Identify the blood parasite species.
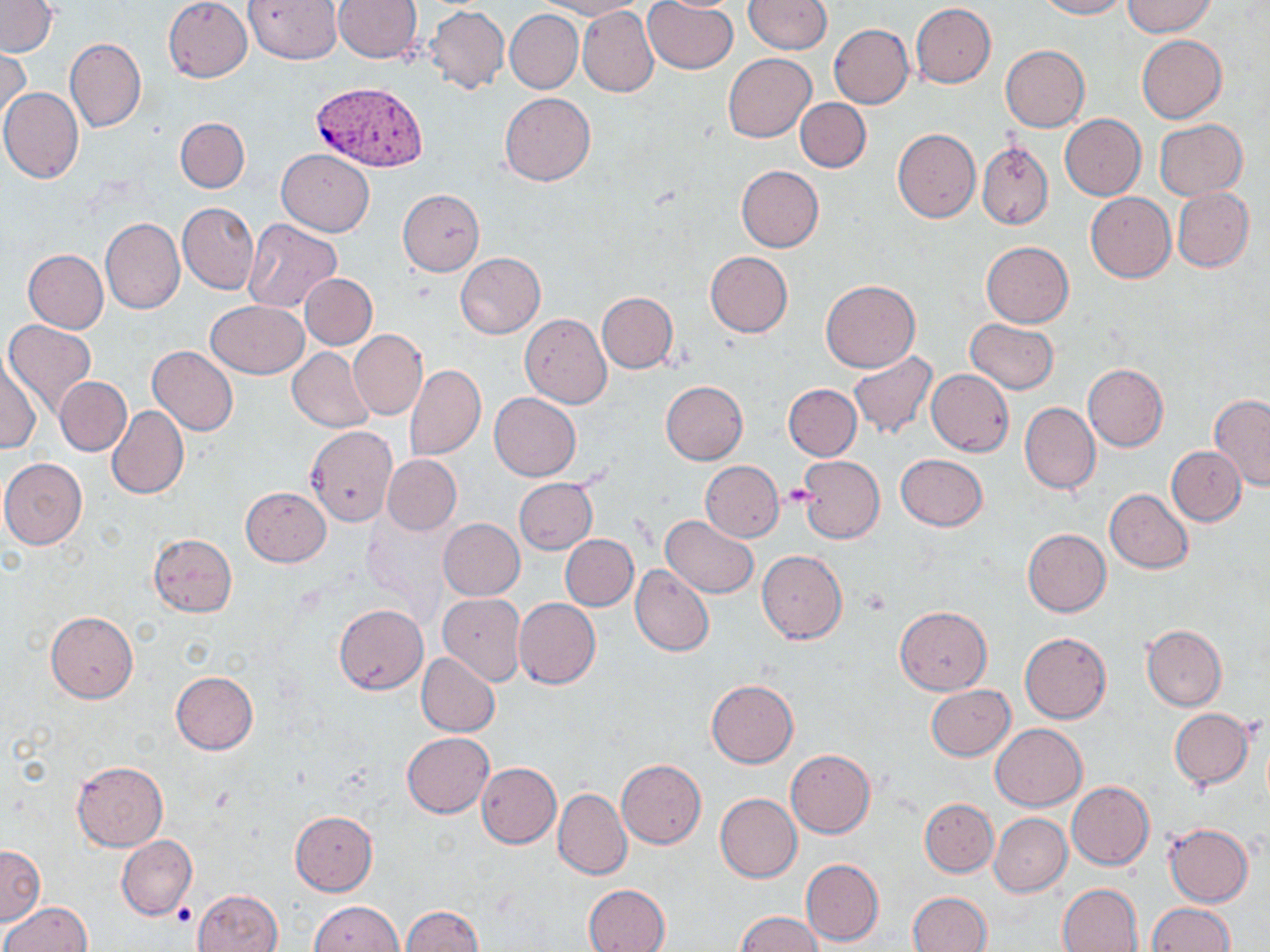

Plasmodium vivax.

uninfected red blood cell locations = approximate bounding boxes as (x1, y1, x2, y2) in pixels: (164, 0, 253, 82), (245, 0, 341, 64), (333, 0, 422, 63), (540, 0, 647, 19), (745, 0, 832, 53), (1036, 0, 1128, 19), (1123, 0, 1216, 36), (0, 1, 57, 57), (644, 1, 738, 73), (911, 3, 996, 88), (578, 5, 658, 97), (424, 6, 509, 93), (506, 10, 583, 93), (829, 24, 913, 108), (1136, 34, 1226, 122), (66, 36, 146, 132), (999, 45, 1089, 133), (1, 49, 31, 130), (723, 53, 816, 143), (0, 87, 83, 183), (499, 92, 596, 186), (796, 98, 871, 172), (1059, 114, 1145, 200), (175, 117, 250, 192), (1154, 119, 1248, 199), (893, 128, 981, 223), (977, 141, 1053, 230), (276, 149, 374, 236), (736, 165, 824, 252), (1171, 187, 1254, 271), (398, 189, 484, 276), (1086, 193, 1175, 282), (178, 202, 258, 294), (100, 217, 185, 315), (242, 219, 342, 312), (981, 242, 1074, 327), (24, 249, 108, 333), (705, 251, 793, 337), (455, 252, 545, 338), (299, 273, 377, 350), (821, 279, 919, 372), (597, 292, 677, 372), (206, 301, 308, 377), (520, 313, 612, 408), (965, 318, 1059, 393), (4, 319, 97, 416), (349, 330, 427, 420), (148, 346, 238, 435), (288, 347, 375, 433), (848, 351, 938, 440), (1, 353, 40, 455), (1082, 364, 1168, 451), (405, 365, 485, 460), (926, 370, 1014, 455), (54, 377, 131, 456), (660, 381, 747, 465), (783, 384, 862, 461), (490, 392, 581, 480), (1209, 395, 1270, 492), (1019, 402, 1100, 494), (107, 405, 188, 500), (306, 425, 399, 527), (1166, 446, 1246, 525), (896, 452, 987, 532), (382, 454, 461, 535), (798, 455, 886, 542), (0, 458, 87, 549), (700, 461, 783, 542), (514, 478, 597, 555), (241, 486, 331, 566), (1104, 489, 1193, 573), (660, 516, 758, 598), (439, 519, 524, 600), (1023, 528, 1111, 616), (149, 533, 237, 616), (560, 534, 639, 611), (757, 550, 847, 644), (630, 564, 714, 656), (437, 593, 526, 686), (513, 598, 601, 689), (334, 604, 427, 694), (894, 606, 991, 695), (45, 612, 138, 703), (1141, 624, 1226, 710), (1019, 632, 1112, 724), (417, 653, 500, 737), (170, 671, 258, 755), (706, 679, 798, 768), (926, 685, 1016, 761), (1168, 708, 1254, 789), (991, 723, 1087, 810), (403, 731, 494, 817), (786, 749, 875, 838), (617, 759, 706, 849), (72, 761, 169, 850), (476, 763, 561, 848), (1067, 780, 1153, 869), (553, 788, 631, 880), (716, 793, 801, 882), (920, 797, 998, 876), (290, 811, 378, 896), (990, 814, 1071, 896), (1164, 823, 1253, 907), (116, 835, 196, 919), (0, 844, 44, 925), (802, 858, 884, 946), (582, 883, 670, 952), (1057, 883, 1143, 952), (194, 888, 283, 952), (908, 892, 991, 952), (309, 901, 403, 952), (2, 902, 91, 952), (1145, 903, 1235, 952), (400, 905, 483, 952), (735, 910, 822, 952)
platelet locations = approximate bounding boxes as (x1, y1, x2, y2) in pixels: (780, 485, 817, 507), (861, 588, 891, 615)
magnification = 1000x
Plasmodium vivax-infected red blood cell locations = approximate bounding boxes as (x1, y1, x2, y2) in pixels: (309, 81, 427, 170)
preparation = thin blood film
image size = 1270×952 pixels
stain = May-Grünwald-Giemsa
modality = optical microscopy
field of view = one of a larger specimen